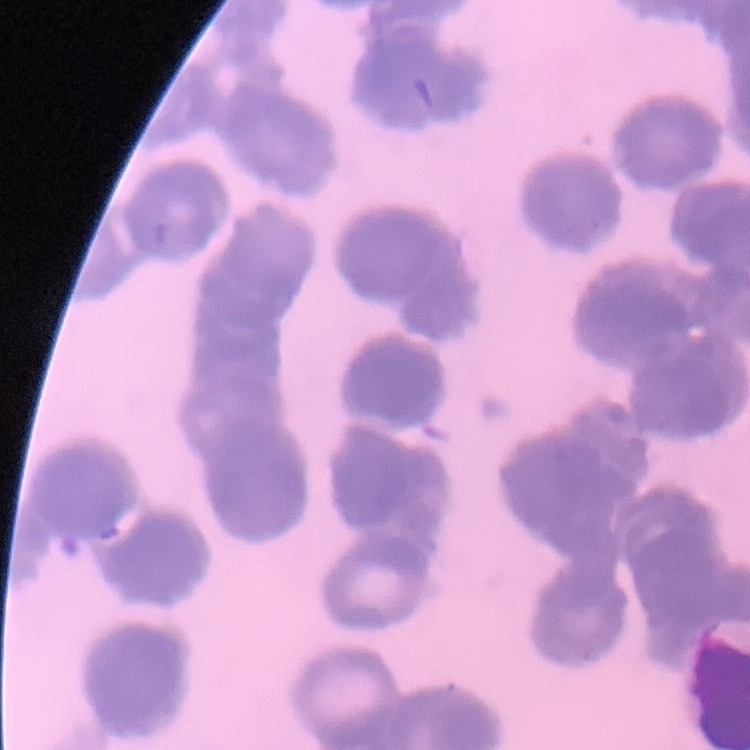 The red blood cells show rouleaux formation. Thin peripheral smear. Field's or Giemsa stain. Square crop of a larger photomicrograph.